Give the position of every Plasmodium parasite.
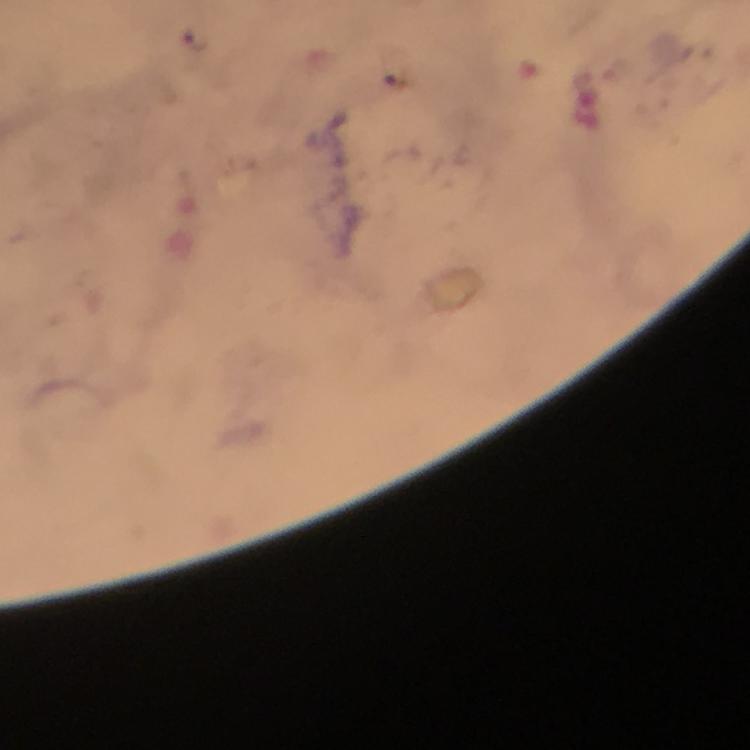
Approximate centers as [x, y] in pixels.
Plasmodium parasites: [196, 42].

Summary:
  - Image size: 750×750 pixels
  - Context: from a malaria diagnostic workup
  - Preparation: thick blood smear
  - Cropped from: a single field of view
  - Immersion oil: used
  - Capture: smartphone camera through the microscope
  - Magnification: 100x
  - Stain: Giemsa